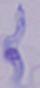
Summary:
  - Identification: trypanosome
  - Modality: photomicrograph
  - Magnification: 1000x